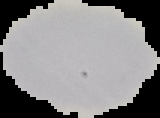

Summary:
  - Image type: segmented cell region with the area outside set to black
  - Result: no malaria parasites detected
  - Preparation: thin blood smear
  - Image size: 160×118 pixels